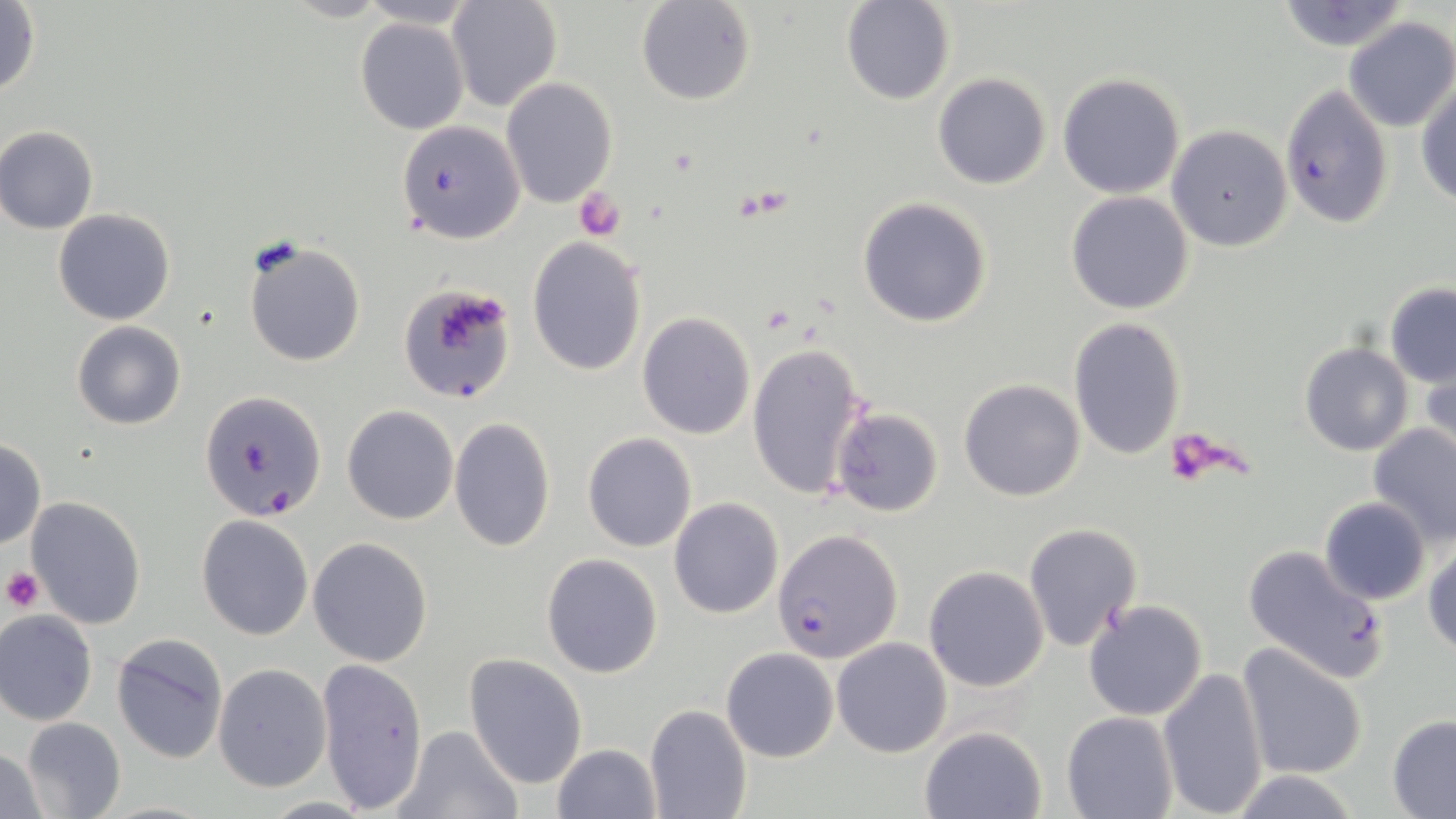
Summary:
  - Coordinate format: approximate bounding boxes as (x1, y1, x2, y2) in pixels
  - Plasmodium falciparum-infected red blood cell locations: (1280, 84, 1395, 230), (399, 281, 516, 404), (200, 390, 327, 521), (774, 529, 902, 664), (1241, 543, 1388, 684)
  - Uninfected red blood cell locations: (446, 0, 563, 112), (636, 0, 758, 106), (840, 2, 955, 104), (1275, 2, 1410, 52), (0, 3, 42, 98), (356, 17, 468, 135), (1342, 17, 1456, 132), (470, 30, 596, 177), (932, 72, 1052, 190), (1058, 72, 1186, 198), (502, 78, 617, 208), (1416, 82, 1456, 205), (398, 120, 527, 242), (1, 126, 100, 234), (1166, 126, 1293, 251), (1066, 190, 1196, 314), (857, 198, 992, 327), (53, 209, 175, 326), (529, 237, 646, 375), (244, 239, 366, 367), (1384, 283, 1456, 387), (638, 312, 755, 439), (1067, 316, 1187, 461), (71, 321, 186, 430), (747, 340, 868, 501), (1299, 342, 1413, 456), (1418, 349, 1456, 462), (971, 350, 1176, 487), (959, 379, 1085, 501), (342, 405, 459, 525), (832, 407, 943, 517), (448, 417, 555, 554), (1368, 423, 1456, 546), (582, 432, 698, 551), (0, 439, 46, 550), (26, 495, 146, 628), (668, 497, 784, 619), (1319, 497, 1431, 605), (197, 514, 313, 640), (1022, 523, 1142, 650), (308, 538, 434, 667), (1423, 541, 1456, 657), (541, 553, 665, 678), (923, 565, 1050, 692), (1084, 599, 1208, 721), (0, 610, 98, 725), (111, 635, 229, 764), (831, 637, 954, 757), (1237, 644, 1369, 781), (721, 647, 837, 761), (464, 654, 588, 789), (314, 657, 426, 811), (213, 664, 331, 792), (1158, 666, 1268, 816), (644, 703, 752, 819), (1061, 710, 1178, 819), (1386, 714, 1456, 817), (19, 717, 127, 819), (394, 725, 523, 819), (920, 726, 1047, 818), (553, 742, 660, 818), (0, 745, 52, 817), (1228, 770, 1363, 818), (261, 796, 372, 817)
  - Platelet locations: (574, 187, 625, 240), (439, 297, 508, 350), (1165, 434, 1228, 482), (2, 567, 42, 612)
  - Slide-level diagnosis: Plasmodium falciparum
  - Image size: 1456×819 pixels
  - Stain: May-Grünwald-Giemsa
  - Magnification: 1000x
  - Preparation: thin blood film
  - Field of view: single
  - Modality: light microscopy